Assess this cell for malaria.
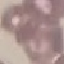

Uninfected.

Summary:
  - Preparation: thin blood film
  - Image type: automatically extracted cell patch, resized to 64 × 64 pixels
  - Capture: smartphone through the microscope eyepiece
  - Stain: Giemsa